Name the cell type shown.
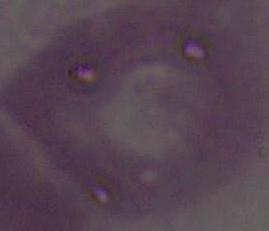
An erythrocyte.

{
  "modality": "photomicrograph",
  "magnification": "1000x"
}